Outline every leukocyte.
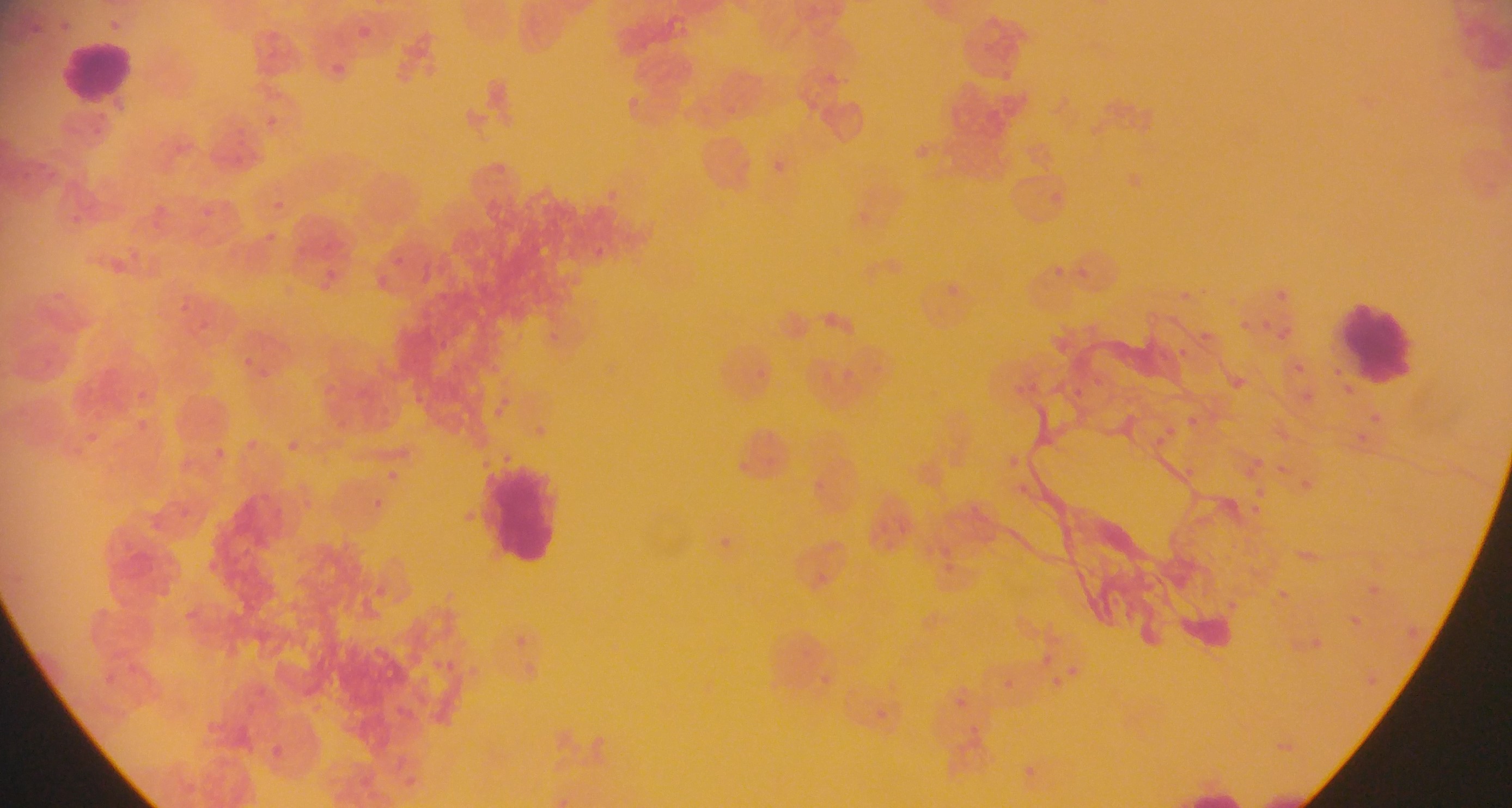

Approximate bounding boxes as [left, top, right, bottom] in pixels.
Leukocytes: [66, 44, 128, 98], [1340, 301, 1415, 383], [484, 466, 554, 564].

Summary:
  - Malaria parasite locations: [358, 27, 372, 37], [335, 63, 345, 72], [267, 115, 276, 126], [275, 199, 285, 212], [203, 212, 217, 215], [265, 231, 277, 240], [393, 257, 404, 264], [325, 270, 335, 279], [321, 282, 331, 290], [1278, 292, 1286, 305], [181, 303, 191, 312], [205, 320, 211, 330], [1236, 321, 1254, 335], [1264, 323, 1272, 334], [1276, 328, 1290, 347], [1179, 347, 1193, 355], [242, 356, 250, 365], [1296, 364, 1309, 374], [1337, 368, 1347, 378], [257, 370, 271, 377], [1092, 380, 1100, 388], [1341, 385, 1354, 396], [1074, 388, 1089, 396], [1301, 389, 1318, 401], [1374, 415, 1381, 423], [1185, 417, 1200, 428], [1165, 425, 1173, 438], [1358, 433, 1367, 442], [1155, 435, 1165, 444], [245, 441, 253, 451], [284, 441, 296, 453], [215, 446, 226, 457], [1185, 467, 1194, 476], [389, 471, 402, 479], [466, 508, 476, 522], [210, 562, 221, 575], [1041, 655, 1053, 665], [129, 664, 143, 674], [1067, 668, 1080, 677], [106, 674, 116, 683], [1052, 675, 1061, 689], [1004, 678, 1017, 688], [955, 696, 969, 708], [398, 705, 406, 716], [873, 706, 888, 722], [970, 726, 979, 735], [271, 743, 282, 755], [1026, 767, 1036, 778] | approximate [x, y] pixel centers of objects too small to bound: [376, 503]
  - Image size: 1512×808 pixels
  - Field of view: single
  - Preparation: thin blood film
  - Capture: mobile-phone photograph through a microscope
  - Country: Ghana